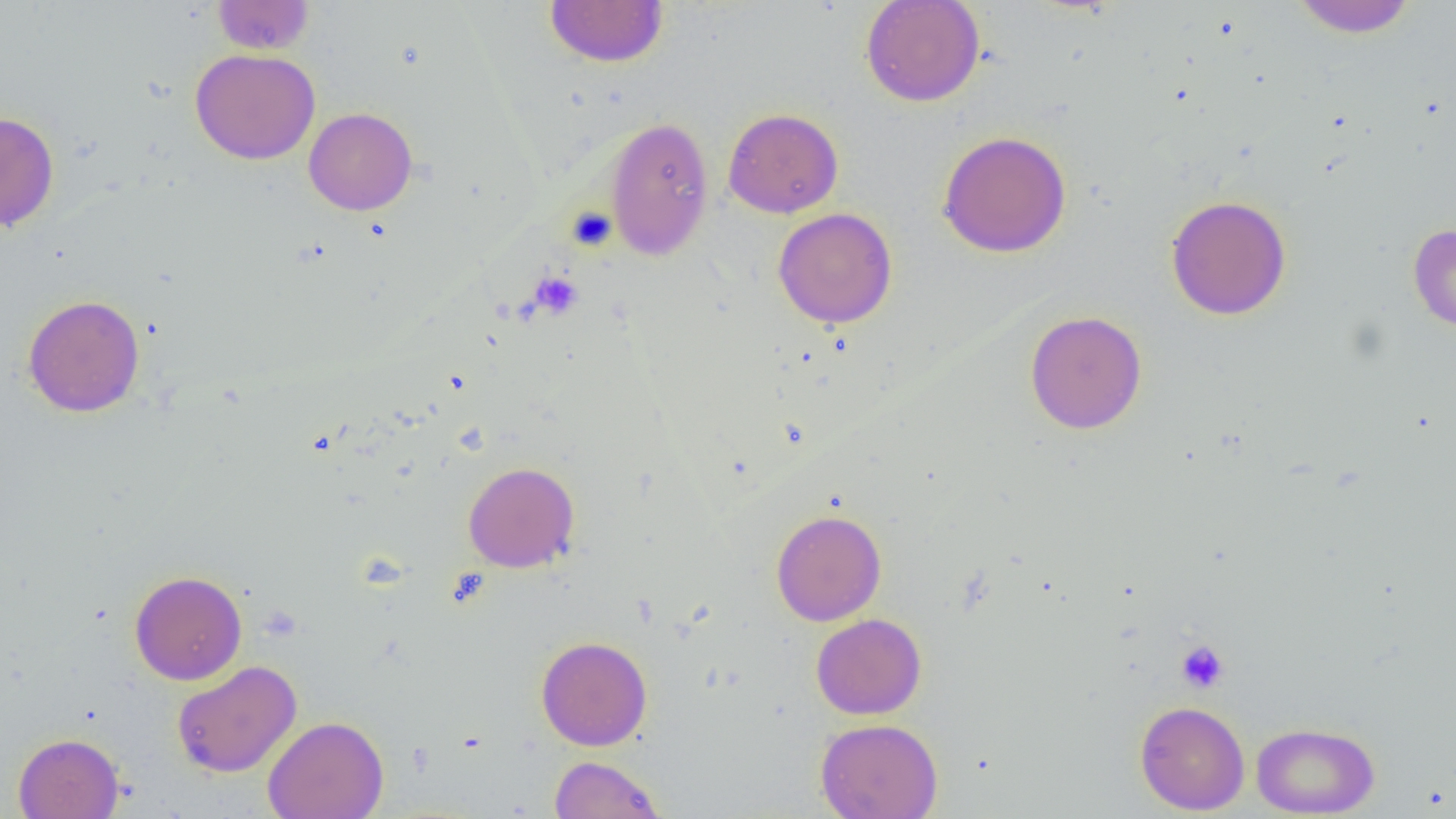

slide-level diagnosis = negative for blood parasites
uninfected red blood cell locations = approximate bounding boxes as named x1/y1/x2/y2 corners in pixels: (x1=212, y1=0, x2=315, y2=55), (x1=544, y1=0, x2=669, y2=67), (x1=860, y1=0, x2=986, y2=107), (x1=1290, y1=0, x2=1417, y2=38), (x1=190, y1=48, x2=320, y2=165), (x1=304, y1=107, x2=417, y2=215), (x1=722, y1=107, x2=844, y2=218), (x1=0, y1=111, x2=59, y2=233), (x1=604, y1=116, x2=714, y2=260), (x1=937, y1=130, x2=1072, y2=257), (x1=1166, y1=194, x2=1292, y2=321), (x1=772, y1=207, x2=897, y2=328), (x1=1408, y1=223, x2=1456, y2=333), (x1=22, y1=294, x2=145, y2=418), (x1=1024, y1=309, x2=1148, y2=434), (x1=463, y1=461, x2=580, y2=573), (x1=771, y1=508, x2=886, y2=626), (x1=129, y1=570, x2=247, y2=685), (x1=811, y1=613, x2=927, y2=719), (x1=536, y1=636, x2=652, y2=751), (x1=171, y1=660, x2=302, y2=778), (x1=1135, y1=700, x2=1250, y2=814), (x1=262, y1=715, x2=389, y2=819), (x1=815, y1=718, x2=943, y2=819), (x1=1251, y1=721, x2=1380, y2=817), (x1=12, y1=732, x2=124, y2=819), (x1=550, y1=755, x2=666, y2=818)
preparation = thin blood smear
field of view = one of a larger specimen
platelet locations = approximate bounding boxes as named x1/y1/x2/y2 corners in pixels: (x1=566, y1=206, x2=617, y2=251), (x1=529, y1=271, x2=583, y2=319), (x1=1176, y1=640, x2=1229, y2=693)
magnification = 1000x
modality = light microscopy
image size = 1456×819 pixels